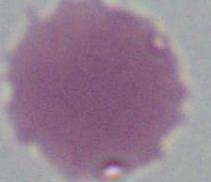
Summary:
  - Identification: erythrocyte
  - Magnification: 1000x
  - Modality: photomicrograph